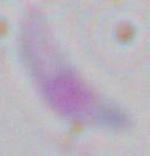 Micrograph. Captured at 1000x magnification. Toxoplasma gondii is seen.